Outline each Plasmodium malariae-infected red blood cell.
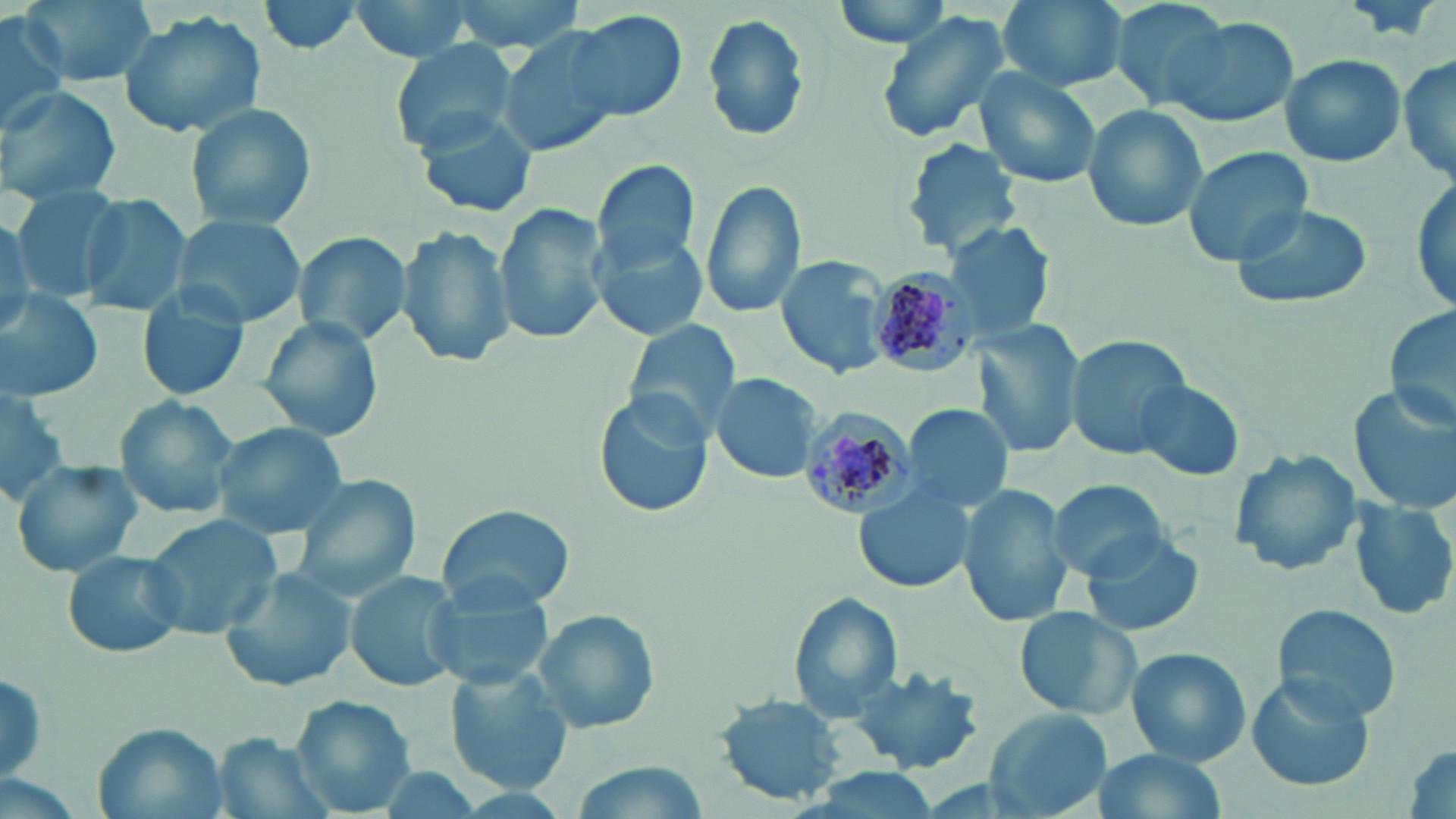

Approximate bounding boxes as named x1/y1/x2/y2 corners in pixels.
Plasmodium malariae-infected red blood cells: (x1=870, y1=272, x2=976, y2=380), (x1=800, y1=414, x2=914, y2=520).

{
  "slide_level_diagnosis": "Plasmodium malariae",
  "stain": "May-Grünwald-Giemsa",
  "modality": "optical microscopy",
  "magnification": "1000x",
  "preparation": "thin blood smear",
  "field_of_view": "single",
  "image_size": "1456×819 pixels",
  "uninfected_red_blood_cell_locations": "approximate bounding boxes as named x1/y1/x2/y2 corners in pixels: (x1=15, y1=0, x2=157, y2=88), (x1=254, y1=0, x2=369, y2=56), (x1=348, y1=0, x2=485, y2=61), (x1=431, y1=0, x2=596, y2=55), (x1=829, y1=0, x2=958, y2=49), (x1=996, y1=0, x2=1130, y2=92), (x1=1106, y1=0, x2=1235, y2=108), (x1=117, y1=10, x2=267, y2=141), (x1=0, y1=11, x2=69, y2=132), (x1=873, y1=11, x2=1014, y2=147), (x1=568, y1=12, x2=686, y2=122), (x1=700, y1=13, x2=811, y2=142), (x1=1162, y1=14, x2=1298, y2=129), (x1=496, y1=27, x2=629, y2=159), (x1=388, y1=40, x2=519, y2=153), (x1=1279, y1=52, x2=1407, y2=169), (x1=1399, y1=53, x2=1456, y2=186), (x1=972, y1=68, x2=1104, y2=191), (x1=1, y1=85, x2=122, y2=202), (x1=183, y1=100, x2=316, y2=231), (x1=1082, y1=102, x2=1207, y2=231), (x1=419, y1=110, x2=541, y2=218), (x1=903, y1=138, x2=1022, y2=255), (x1=1182, y1=145, x2=1314, y2=266), (x1=592, y1=159, x2=701, y2=275), (x1=1411, y1=170, x2=1455, y2=316), (x1=699, y1=179, x2=806, y2=320), (x1=4, y1=186, x2=116, y2=304), (x1=74, y1=191, x2=194, y2=317), (x1=495, y1=201, x2=610, y2=344), (x1=1226, y1=201, x2=1375, y2=311), (x1=0, y1=213, x2=36, y2=338), (x1=170, y1=213, x2=306, y2=326), (x1=943, y1=216, x2=1060, y2=343), (x1=396, y1=225, x2=514, y2=369), (x1=592, y1=229, x2=707, y2=341), (x1=293, y1=230, x2=411, y2=348), (x1=776, y1=254, x2=892, y2=378), (x1=136, y1=287, x2=253, y2=403), (x1=0, y1=290, x2=104, y2=400), (x1=1383, y1=307, x2=1456, y2=433), (x1=257, y1=315, x2=383, y2=442), (x1=623, y1=320, x2=740, y2=438), (x1=974, y1=322, x2=1086, y2=459), (x1=1064, y1=335, x2=1194, y2=460), (x1=709, y1=373, x2=824, y2=483), (x1=1133, y1=379, x2=1247, y2=480), (x1=0, y1=385, x2=71, y2=498), (x1=1351, y1=386, x2=1456, y2=515), (x1=594, y1=390, x2=712, y2=519), (x1=113, y1=396, x2=241, y2=519), (x1=905, y1=404, x2=1014, y2=513), (x1=214, y1=422, x2=348, y2=537), (x1=1228, y1=449, x2=1359, y2=578), (x1=11, y1=460, x2=145, y2=578), (x1=290, y1=474, x2=420, y2=601), (x1=1048, y1=478, x2=1174, y2=581), (x1=957, y1=482, x2=1074, y2=628), (x1=854, y1=487, x2=975, y2=595), (x1=1352, y1=495, x2=1456, y2=621), (x1=435, y1=504, x2=576, y2=613), (x1=139, y1=515, x2=281, y2=639), (x1=1079, y1=529, x2=1207, y2=639), (x1=60, y1=547, x2=190, y2=661), (x1=218, y1=566, x2=360, y2=695), (x1=344, y1=569, x2=465, y2=694), (x1=423, y1=580, x2=554, y2=691), (x1=787, y1=593, x2=903, y2=722), (x1=1272, y1=603, x2=1401, y2=722), (x1=1015, y1=606, x2=1141, y2=721), (x1=530, y1=608, x2=662, y2=735), (x1=1126, y1=647, x2=1251, y2=765), (x1=845, y1=666, x2=986, y2=775), (x1=1, y1=667, x2=49, y2=782), (x1=445, y1=668, x2=573, y2=792), (x1=1243, y1=675, x2=1376, y2=795), (x1=716, y1=694, x2=846, y2=803), (x1=290, y1=696, x2=416, y2=814), (x1=985, y1=708, x2=1108, y2=816), (x1=94, y1=725, x2=225, y2=815), (x1=214, y1=733, x2=332, y2=819), (x1=1089, y1=748, x2=1229, y2=819)"
}